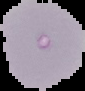
Malaria status: uninfected. From a thin blood film. Image is 85×91 pixels. The area outside the segmented cell region is set to black.